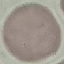

malaria status = uninfected
stain = Giemsa
image type = cell patch, automatically extracted from a larger field of view and resized to 64 × 64 pixels
preparation = thin blood smear
capture = smartphone through the microscope eyepiece